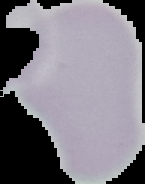
Summary:
  - Result: no Plasmodium parasites detected
  - Image size: 145×184 pixels
  - Preparation: thin blood smear
  - Image type: segmented cell region with the area outside set to black